Outline each Plasmodium falciparum parasite and classify it by life-cycle stage.
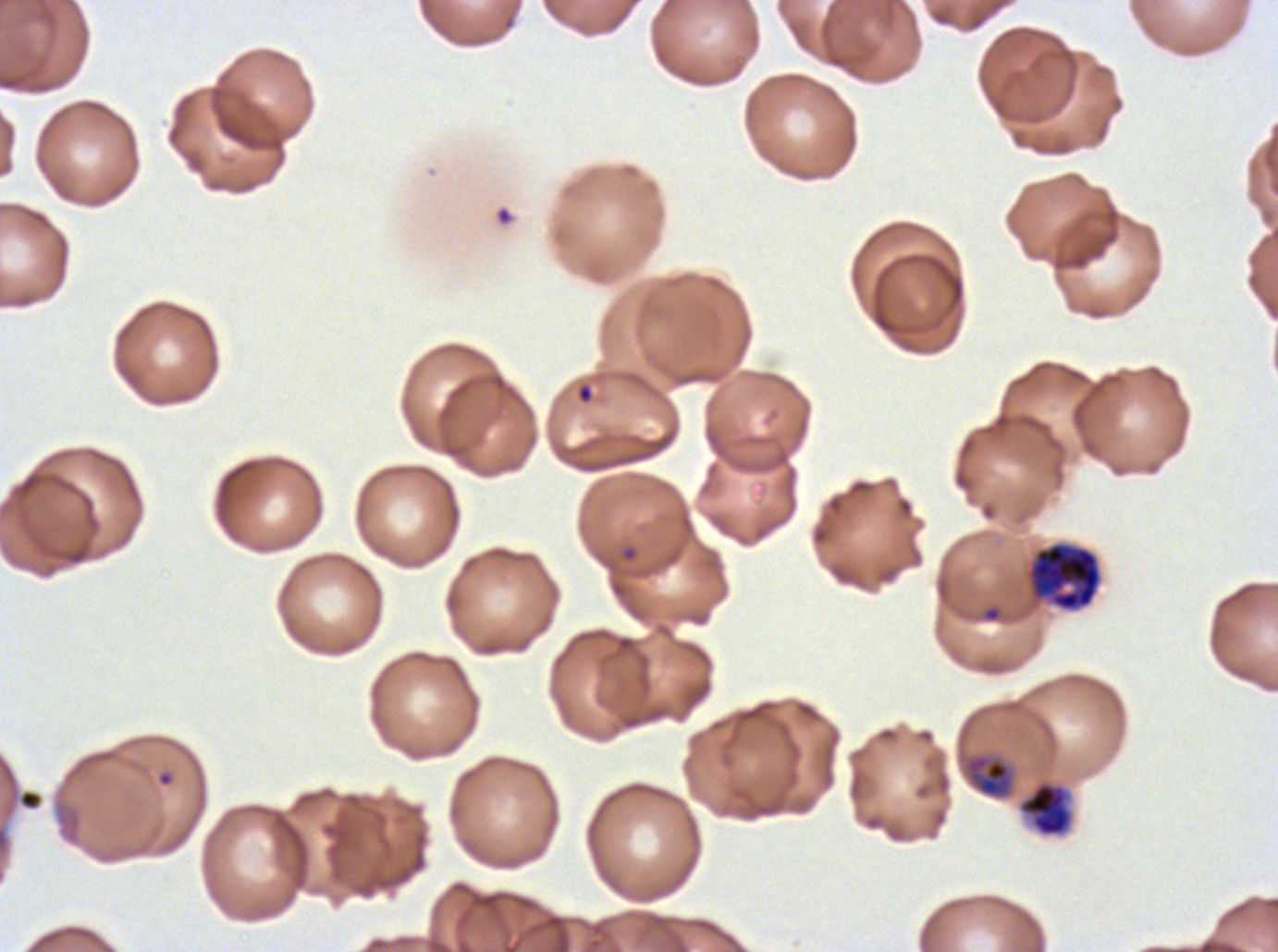

Approximate bounding rectangles given as corner coordinates in pixels from the top-left.
Rings: (x1=576, y1=383, x2=595, y2=405), (x1=621, y1=545, x2=638, y2=562).
Late-ring/early-trophozoite forms: (x1=963, y1=752, x2=1016, y2=800).
One object is labeled both ring and early schizont by the source: (x1=1024, y1=541, x2=1103, y2=613).
No mid trophozoites, late trophozoites, late schizonts, segmenters, or gametocytes observed.

stain = Giemsa
life-cycle stages observed = ring, late-ring/early-trophozoite
field of view = one sub-image of a larger composite
image size = 1278×952 pixels
specimen = Plasmodium falciparum cultured ex vivo for 24 to 48 hours, from a patient in The Gambia
preparation = thin blood smear